Outline each blood parasite and name the species.
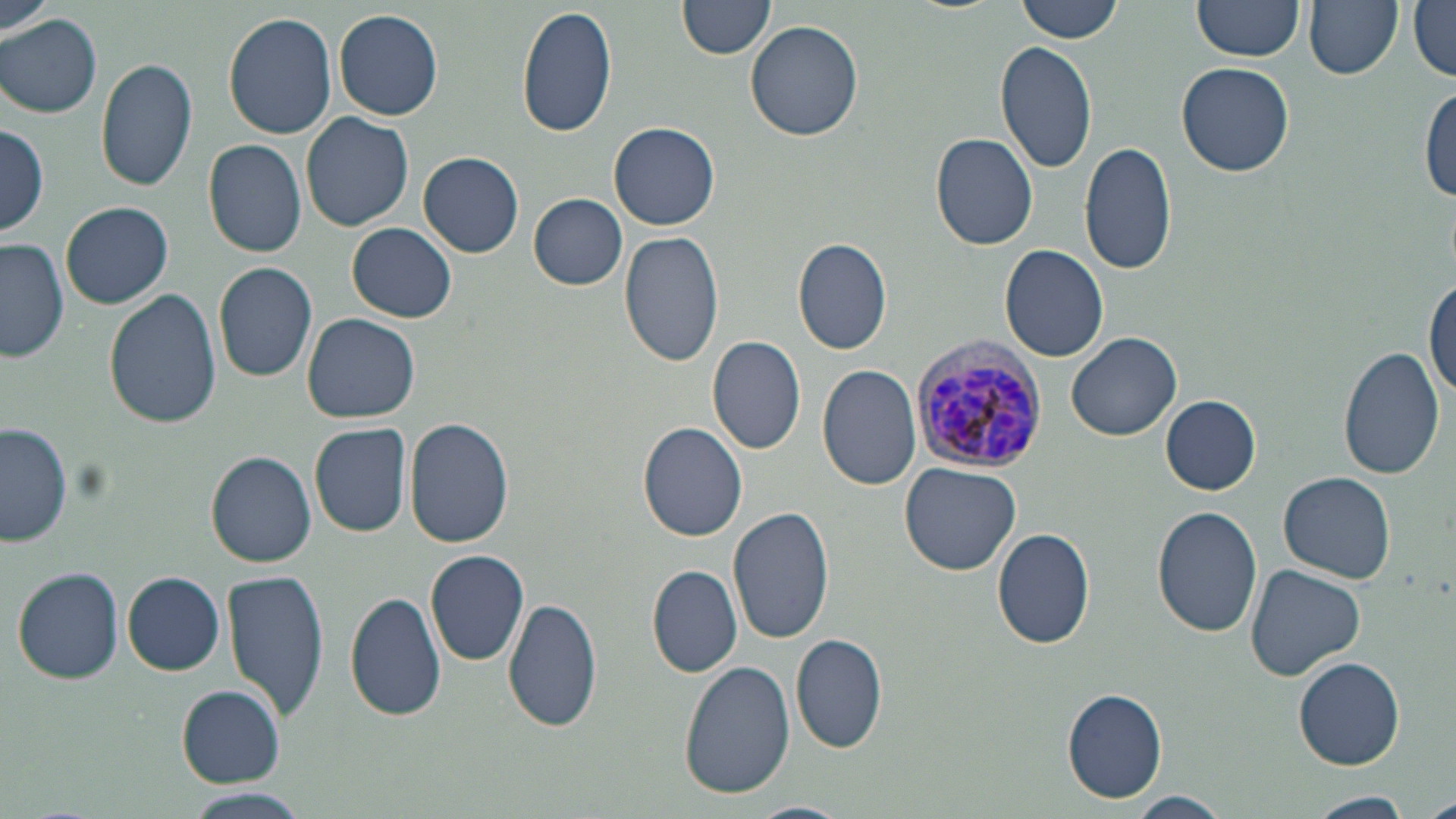
Approximate bounding boxes as (x1,y1)-(x2,y2) corner pairs in pixels.
Plasmodium vivax-infected red blood cells: (907,340)-(1052,474).
No Plasmodium falciparum, Plasmodium ovale, Plasmodium malariae, Babesia divergens, or Trypanosoma brucei observed.

slide-level diagnosis = Plasmodium vivax
image size = 1456×819 pixels
uninfected red blood cell locations = approximate bounding boxes as (x1,y1)-(x2,y2) corner pairs in pixels: (679,0)-(776,60), (1017,0)-(1124,43), (1302,0)-(1404,81), (1409,0)-(1455,82), (1191,1)-(1303,64), (1,3)-(56,41), (518,5)-(618,140), (333,8)-(443,120), (223,11)-(338,139), (0,14)-(102,117), (744,21)-(862,141), (995,39)-(1099,175), (95,57)-(198,193), (1177,61)-(1294,176), (1419,86)-(1455,203), (300,111)-(414,231), (610,122)-(721,231), (0,123)-(50,238), (928,131)-(1041,251), (203,138)-(309,257), (1080,140)-(1179,276), (418,150)-(524,257), (530,193)-(627,289), (61,202)-(173,309), (346,223)-(458,323), (619,230)-(725,366), (0,238)-(68,363), (792,238)-(894,355), (999,244)-(1110,363), (212,262)-(318,384), (1425,278)-(1455,404), (104,287)-(222,431), (302,312)-(419,423), (1067,331)-(1183,440), (707,335)-(807,456), (1339,347)-(1446,483), (817,364)-(921,490), (1161,395)-(1261,494), (405,417)-(515,547), (0,421)-(75,551), (309,422)-(411,539), (637,422)-(750,542), (206,450)-(316,567), (900,462)-(1021,576), (1279,471)-(1397,583), (727,505)-(835,645), (1152,505)-(1264,638), (991,527)-(1097,650), (425,550)-(531,666), (1243,564)-(1366,682), (647,565)-(743,677), (12,567)-(125,686), (223,568)-(329,721), (122,572)-(225,676), (345,590)-(445,721), (503,597)-(602,737), (792,634)-(890,753), (1294,657)-(1406,770), (679,660)-(795,798), (177,686)-(286,786), (1062,688)-(1169,804), (183,791)-(311,819), (1307,791)-(1414,818), (1126,792)-(1231,819), (1422,794)-(1456,819), (744,800)-(850,819)
stain = May-Grünwald-Giemsa
preparation = thin blood smear
modality = light microscopy
field of view = single
magnification = 1000x